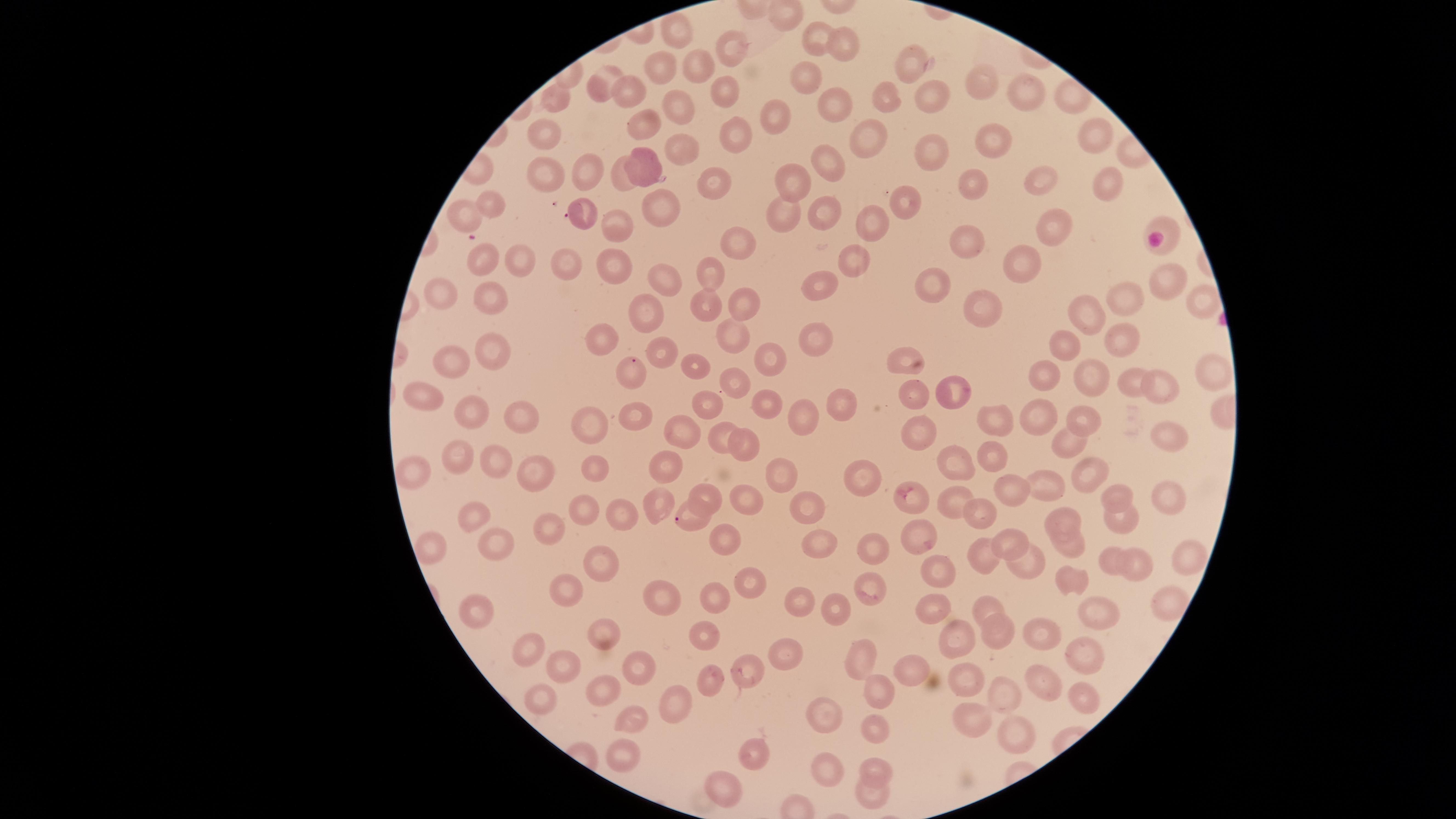
Approximate marker points as [x, y] in pixels. Parasitized red blood cells: [567, 218], [633, 361], [699, 519]. Uninfected red blood cells: [675, 29], [811, 32], [845, 47], [739, 53], [700, 61], [913, 65], [662, 66], [805, 76], [600, 82], [983, 83], [632, 84], [719, 85], [886, 95], [930, 95], [1027, 96], [828, 97], [555, 98], [676, 102], [772, 109], [636, 124], [543, 129], [735, 132], [991, 136], [875, 137], [1097, 141], [680, 143], [931, 150], [835, 158], [646, 160], [585, 169], [549, 173], [621, 173], [1043, 181], [798, 182], [1107, 182], [970, 183], [713, 184], [493, 202], [907, 203], [664, 204], [784, 209], [822, 209], [467, 213], [872, 221], [609, 223], [1164, 225], [1060, 226], [965, 239], [733, 245], [854, 258], [1026, 259], [486, 262], [517, 263], [564, 265], [615, 268], [665, 273], [710, 273], [820, 283], [931, 284], [1164, 284], [490, 292], [442, 296], [1130, 301], [1201, 303], [708, 306], [983, 307], [748, 309], [650, 311], [1087, 315], [597, 334], [733, 334], [813, 334], [1122, 338], [1066, 341], [488, 350], [664, 350], [778, 360], [904, 360], [454, 364], [693, 364], [1210, 373], [1044, 375], [1086, 376], [1128, 380], [737, 382], [1161, 387], [950, 391], [920, 394], [426, 395], [771, 400], [705, 404], [843, 404], [476, 409], [520, 413], [803, 413], [998, 417], [1082, 417], [633, 418], [1042, 418], [592, 423], [679, 429], [1166, 432], [717, 434], [920, 435], [1068, 437], [745, 445], [993, 455], [456, 459], [596, 462], [490, 463], [955, 464], [669, 466], [868, 466], [413, 468], [1082, 468], [530, 469], [783, 473], [1046, 483], [1006, 488], [1169, 491], [709, 494], [1120, 495], [951, 498], [815, 499], [916, 499], [653, 501], [752, 501], [582, 509], [626, 512], [980, 514], [474, 515], [1119, 515], [1060, 518], [555, 526], [728, 536], [921, 537], [495, 538], [1011, 541], [815, 545], [1072, 545], [871, 546], [432, 551], [601, 557], [982, 559], [1133, 559], [1183, 559], [1111, 562], [1020, 563], [935, 572], [1072, 573], [748, 574], [867, 580], [577, 586], [719, 598], [802, 598], [1171, 598], [662, 600], [839, 605], [929, 605], [987, 605], [1095, 612], [477, 614], [996, 631], [951, 632], [1043, 632], [601, 633], [705, 636], [788, 649], [1077, 652], [528, 653], [560, 663], [856, 663], [635, 669], [747, 669], [909, 670], [963, 674], [710, 678], [1045, 681], [599, 684], [884, 692], [1005, 697], [1075, 697], [541, 698], [679, 705], [970, 713], [625, 716], [820, 717], [872, 726], [1010, 733], [622, 749], [752, 753], [880, 765], [827, 774], [731, 785], [873, 792]. One field of view of the specimen. Image is 1456×819 pixels. Species: Plasmodium falciparum. Photographed with a smartphone camera through the microscope eyepiece. Giemsa-stained preparation. Presence: malaria parasites identified. The visible region is circular. Thin smear of blood.